Locate every white blood cell.
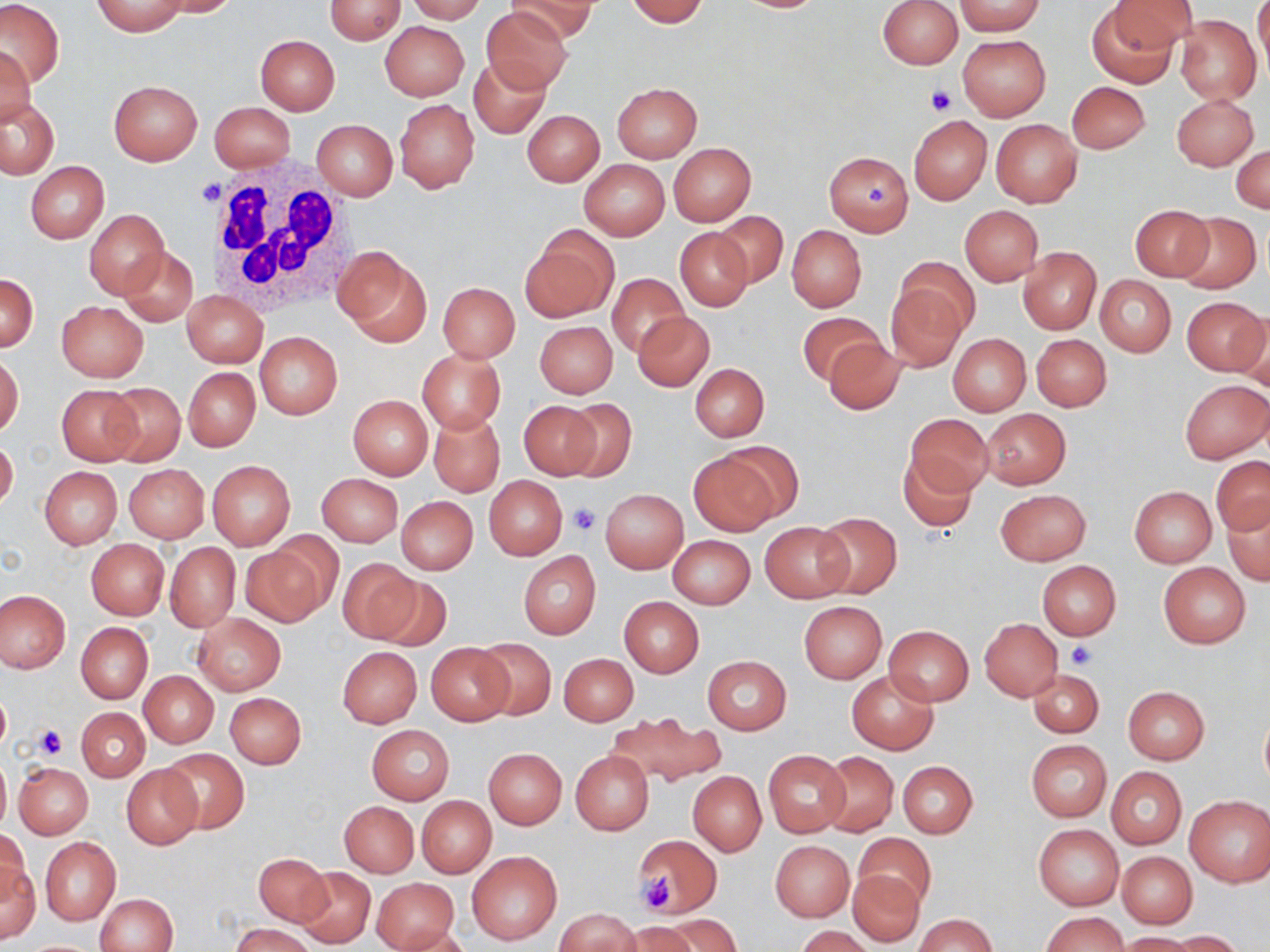

Approximate bounding boxes as [x1, y1, x2, y2] in pixels.
White blood cells: [202, 159, 358, 319].

Summary:
  - Platelet locations: [924, 85, 956, 116], [198, 177, 223, 208], [862, 181, 891, 212], [568, 504, 601, 537], [1066, 640, 1097, 668], [33, 724, 66, 760], [632, 873, 678, 914]
  - Uninfected red blood cell locations: [153, 0, 240, 17], [325, 0, 406, 44], [406, 0, 487, 23], [509, 0, 595, 44], [625, 0, 710, 26], [730, 0, 832, 13], [1111, 0, 1198, 53], [1255, 0, 1269, 84], [0, 1, 63, 88], [876, 1, 963, 69], [92, 2, 189, 36], [955, 2, 1045, 36], [1087, 3, 1180, 87], [482, 5, 573, 93], [1174, 16, 1261, 104], [379, 21, 469, 100], [957, 34, 1050, 120], [255, 36, 340, 115], [0, 44, 36, 127], [469, 57, 550, 137], [108, 80, 202, 165], [1068, 81, 1151, 154], [612, 82, 702, 162], [1171, 93, 1258, 171], [1, 97, 60, 178], [395, 99, 479, 193], [211, 102, 295, 173], [521, 109, 604, 186], [908, 115, 992, 206], [991, 119, 1082, 208], [312, 120, 397, 201], [668, 143, 755, 226], [1232, 145, 1269, 215], [824, 151, 914, 235], [579, 159, 669, 241], [25, 161, 109, 243], [1131, 205, 1213, 281], [960, 206, 1044, 286], [84, 209, 170, 300], [714, 211, 788, 288], [1175, 213, 1261, 293], [787, 226, 866, 311], [675, 227, 754, 311], [521, 232, 616, 323], [334, 245, 432, 347], [1018, 247, 1101, 334], [119, 248, 198, 325], [898, 256, 978, 335], [608, 274, 689, 356], [1095, 274, 1176, 356], [0, 275, 38, 350], [437, 281, 520, 362], [884, 281, 968, 371], [182, 290, 268, 367], [1181, 296, 1269, 377], [56, 301, 147, 382], [633, 311, 713, 391], [797, 312, 882, 385], [1235, 312, 1270, 392], [534, 320, 618, 398], [255, 333, 342, 419], [947, 333, 1031, 416], [1031, 334, 1111, 411], [823, 338, 906, 415], [417, 349, 506, 434], [1, 355, 23, 436], [690, 364, 768, 441], [182, 368, 260, 451], [1179, 379, 1270, 462], [103, 383, 185, 467], [57, 385, 140, 465], [348, 395, 433, 479], [560, 398, 637, 481], [518, 400, 606, 480], [989, 408, 1079, 565], [981, 409, 1071, 488], [428, 410, 505, 497], [906, 413, 992, 496], [0, 439, 17, 511], [717, 442, 804, 522], [897, 451, 977, 532], [689, 453, 781, 536], [1212, 457, 1270, 533], [206, 460, 295, 550], [123, 464, 209, 542], [40, 466, 122, 548], [316, 473, 404, 546], [484, 475, 568, 560], [1130, 487, 1216, 566], [601, 489, 688, 572], [995, 489, 1091, 565], [396, 496, 478, 574], [1222, 497, 1270, 585], [813, 512, 901, 599], [760, 522, 852, 602], [667, 534, 755, 608], [86, 539, 170, 620], [165, 543, 240, 632], [241, 544, 331, 628], [518, 551, 600, 640], [338, 559, 421, 644], [1036, 560, 1121, 640], [1159, 563, 1251, 647], [366, 574, 454, 653], [0, 591, 70, 671], [620, 597, 704, 676], [798, 600, 887, 682], [193, 614, 286, 694], [980, 619, 1062, 701], [76, 622, 153, 703], [884, 626, 974, 705], [475, 638, 556, 720], [426, 643, 513, 725], [338, 648, 421, 727], [560, 653, 638, 725], [702, 655, 792, 734], [1029, 668, 1103, 737], [140, 670, 218, 747], [846, 670, 937, 755], [1122, 685, 1210, 764], [0, 689, 11, 754], [225, 692, 306, 768], [76, 707, 150, 782], [1259, 708, 1270, 792], [607, 711, 723, 788], [367, 724, 455, 805], [1025, 740, 1111, 822], [484, 748, 567, 828], [158, 749, 249, 834], [763, 750, 851, 836], [571, 751, 654, 834], [818, 751, 898, 836], [0, 755, 11, 833], [897, 760, 978, 838], [15, 761, 93, 839], [122, 765, 203, 848], [1107, 767, 1186, 850], [689, 772, 765, 855], [1184, 795, 1269, 887], [417, 796, 496, 878], [340, 802, 419, 877], [1034, 824, 1124, 911], [1, 829, 32, 902], [853, 833, 935, 911], [632, 834, 723, 919], [41, 837, 120, 925], [770, 841, 854, 921], [466, 850, 562, 946], [1117, 851, 1197, 928], [253, 852, 331, 927], [1, 861, 41, 945], [293, 867, 375, 948], [847, 869, 924, 947], [371, 877, 460, 952], [96, 893, 178, 952], [556, 908, 641, 952], [1041, 911, 1128, 951], [658, 914, 740, 952], [915, 914, 996, 951], [231, 921, 317, 952], [621, 923, 700, 952], [387, 925, 472, 952], [795, 926, 875, 952], [1166, 931, 1246, 951], [1119, 932, 1203, 952], [20, 939, 103, 951]
  - Slide-level diagnosis: no evidence of blood parasites
  - Preparation: thin blood film
  - Modality: optical microscopy
  - Image size: 1270×952 pixels
  - Magnification: 1000x
  - Field of view: one of a larger specimen
  - Stain: May-Grünwald-Giemsa